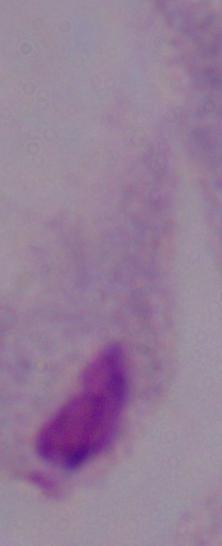

identification = trichomonad
modality = photomicrograph
magnification = 1000x